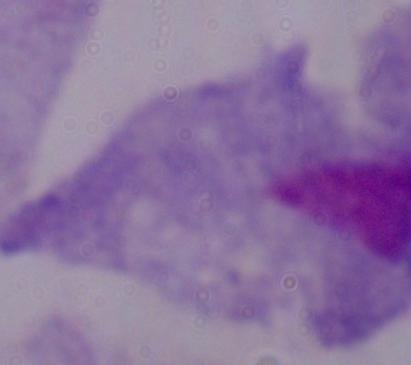

magnification = 1000x
modality = photomicrograph
identification = trichomonad